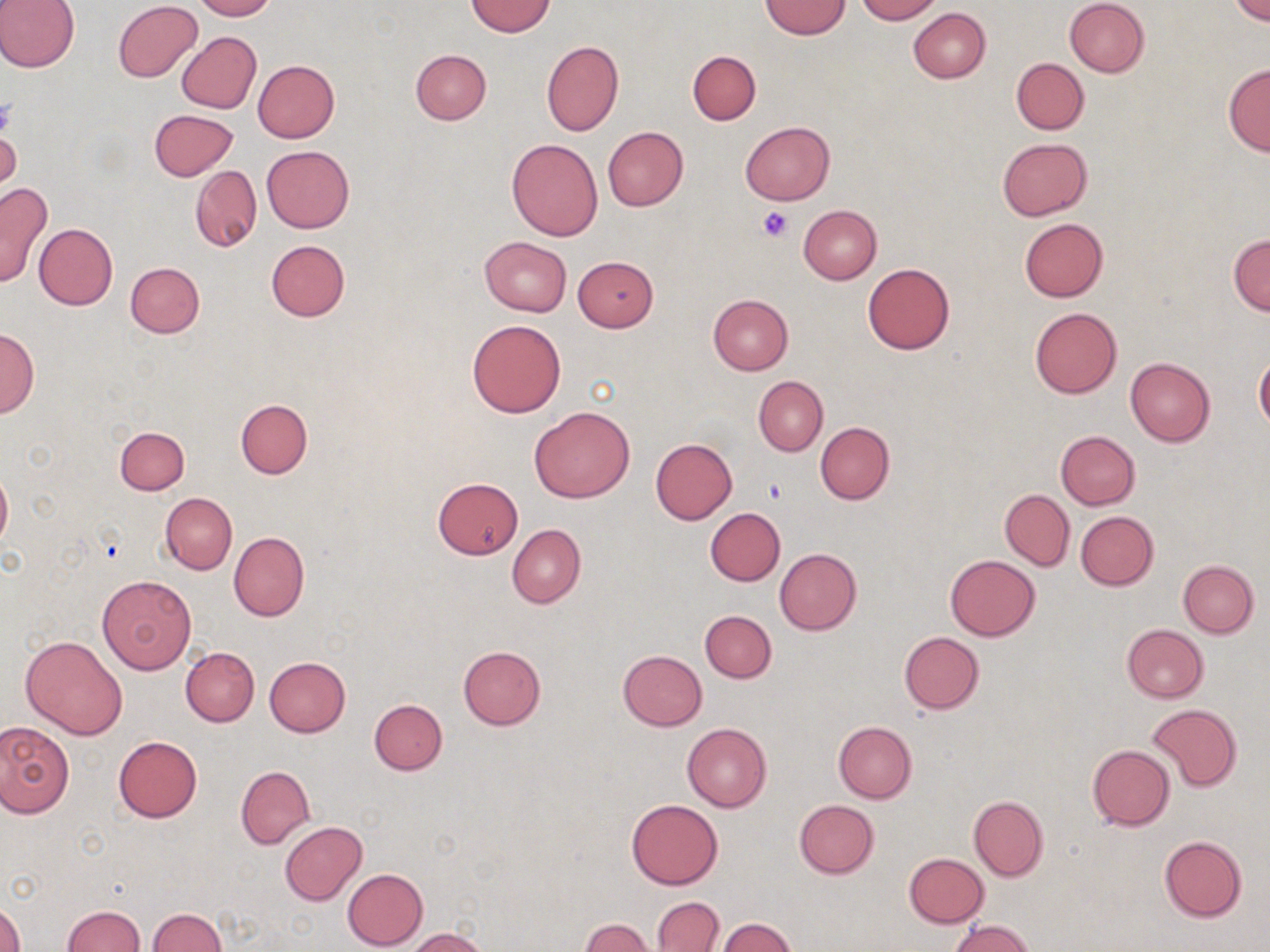

Summary:
  - Coordinate format: approximate bounding boxes as (x1,y1)-(x2,y2) corner pairs in pixels
  - Uninfected red blood cell locations: (0,0)-(79,73), (190,0)-(275,20), (854,0)-(940,23), (1065,0)-(1149,77), (1232,0)-(1269,25), (465,1)-(556,36), (760,1)-(850,39), (113,2)-(203,83), (909,7)-(990,83), (177,32)-(261,114), (542,40)-(623,136), (409,48)-(491,125), (687,50)-(761,125), (1012,58)-(1088,134), (252,59)-(340,142), (1223,63)-(1270,156), (148,109)-(238,181), (741,121)-(835,205), (603,126)-(689,211), (0,128)-(21,195), (996,138)-(1093,221), (507,139)-(603,240), (261,145)-(353,232), (191,166)-(261,251), (0,182)-(51,287), (799,205)-(881,284), (1019,218)-(1108,301), (33,223)-(117,310), (1228,235)-(1269,316), (479,236)-(572,316), (265,240)-(350,322), (572,256)-(660,331), (125,262)-(204,338), (862,264)-(955,354), (707,295)-(792,375), (1029,306)-(1123,399), (467,319)-(566,417), (1,328)-(39,417), (1254,355)-(1270,431), (1125,357)-(1214,446), (753,376)-(827,456), (234,399)-(313,479), (529,405)-(634,503), (814,423)-(894,505), (115,425)-(189,495), (1056,431)-(1141,509), (650,438)-(737,523), (0,465)-(11,551), (432,477)-(523,559), (1000,489)-(1075,571), (160,493)-(237,574), (975,496)-(1071,621), (705,507)-(785,586), (1075,511)-(1158,590), (507,524)-(585,608), (229,531)-(309,622), (774,548)-(862,635), (945,555)-(1040,641), (1178,560)-(1258,638), (97,575)-(196,674), (700,610)-(776,683), (1121,624)-(1209,702), (899,631)-(984,714), (20,634)-(128,740), (458,646)-(546,730), (180,647)-(259,726), (618,650)-(707,730), (264,656)-(350,736), (369,698)-(447,775), (1148,704)-(1241,792), (0,721)-(73,817), (834,721)-(917,802), (682,722)-(771,812), (113,736)-(201,821), (1087,745)-(1175,831), (235,766)-(314,848), (968,795)-(1049,881), (627,799)-(723,889), (794,800)-(878,878), (279,821)-(366,904), (1159,836)-(1247,922), (904,853)-(990,927), (341,868)-(428,951), (652,897)-(723,952), (0,902)-(25,952), (61,905)-(145,951), (148,908)-(225,952), (718,918)-(797,952), (580,919)-(654,952), (949,920)-(1037,952), (407,928)-(488,952)
  - Platelet locations: (0,98)-(16,139), (757,205)-(792,241), (763,478)-(787,504)
  - Slide-level diagnosis: no evidence of blood parasites
  - Image size: 1270×952 pixels
  - Field of view: single
  - Preparation: thin blood smear
  - Magnification: 1000x
  - Modality: light microscopy
  - Stain: May-Grünwald-Giemsa